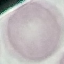 Result: no malaria parasites detected. Acquired by smartphone through the microscope eyepiece. Cell patch, automatically extracted from a larger field of view and resized to 64 × 64 pixels. Giemsa stain. Thin smear of blood.